Classify this cell by malaria status.
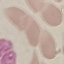

Uninfected.

Automatically extracted cell patch, resized to 64 × 64 pixels. Giemsa stain. Acquired by smartphone through the microscope eyepiece. Thin smear of blood.